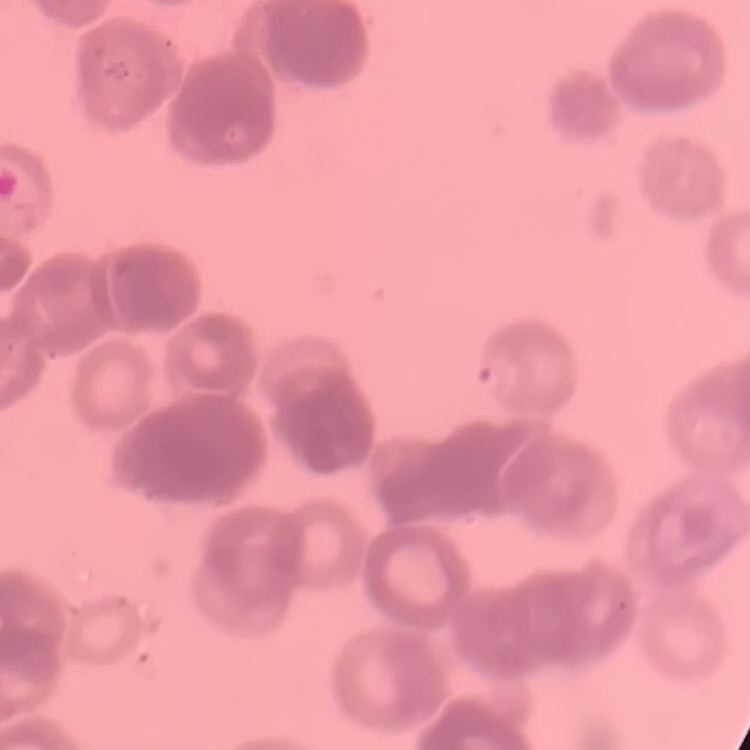

Summary:
  - Red blood cell morphology: rouleaux formation
  - Stain: Field's or Giemsa
  - Preparation: thin blood film
  - Image type: one tile cut from a larger photomicrograph